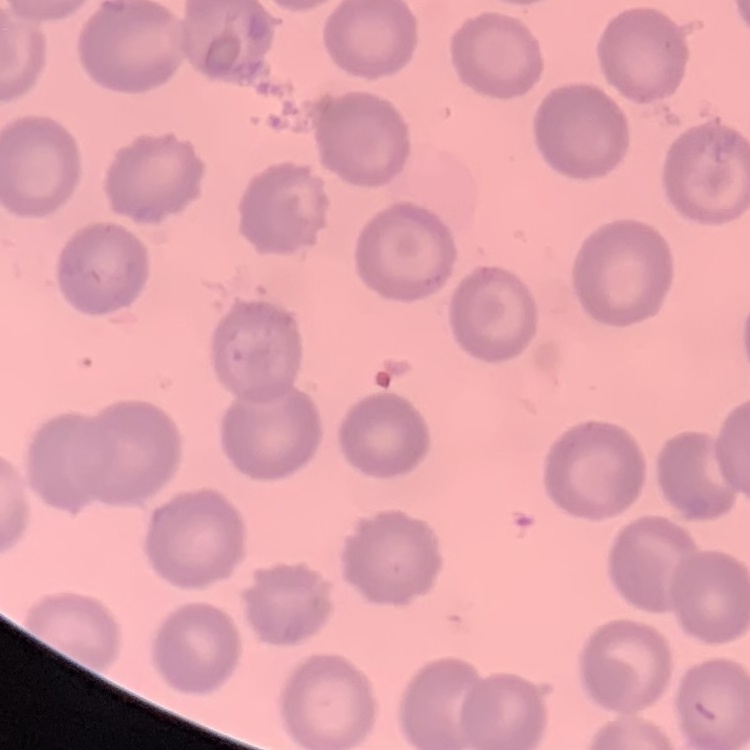

Summary:
  - Erythrocyte morphology: no rouleaux formation
  - Stain: Field's or Giemsa
  - Preparation: thin blood smear
  - Image type: square crop of a larger photomicrograph